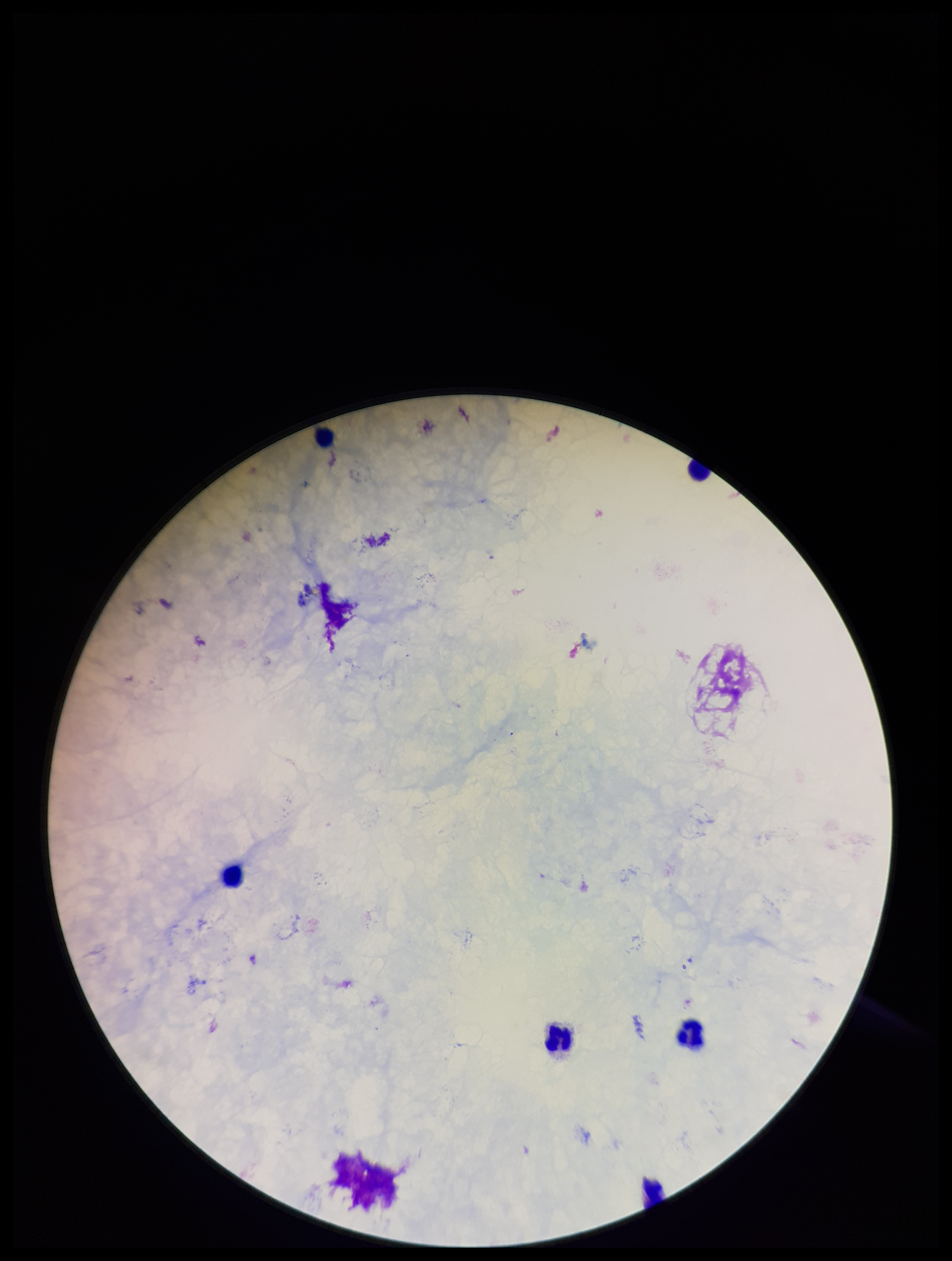

plasmodium_parasites: none detected
stain: Giemsa
image_size: 952×1261 pixels
capture: smartphone photograph through the microscope eyepiece
patient_malaria_status: negative
preparation: thick blood smear
field_of_view: one from this slide
parasite_count: 0
leukocyte_count: 6